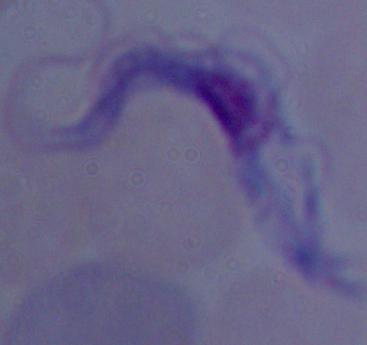
A trypanosome is shown. Photomicrograph. Captured at 1000x magnification.